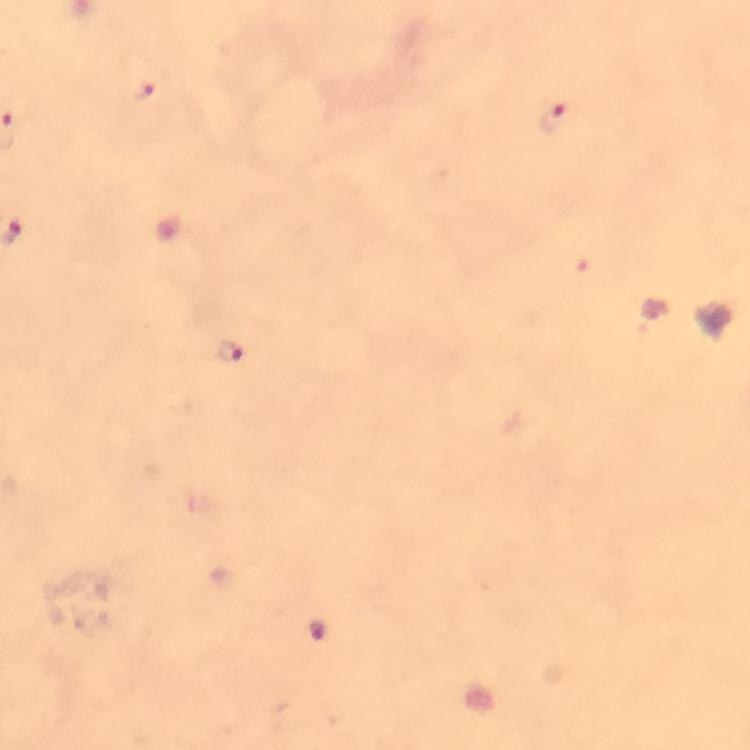
preparation = thick smear
magnification = 100x
cropped from = a single field of view
image size = 750×750 pixels
stain = Giemsa
immersion oil = used
capture = smartphone photograph through a microscope
malaria parasite locations = approximate centers as [x, y] in pixels: [142, 91], [554, 117], [234, 354], [317, 630]
context = from a diagnostic examination for malaria